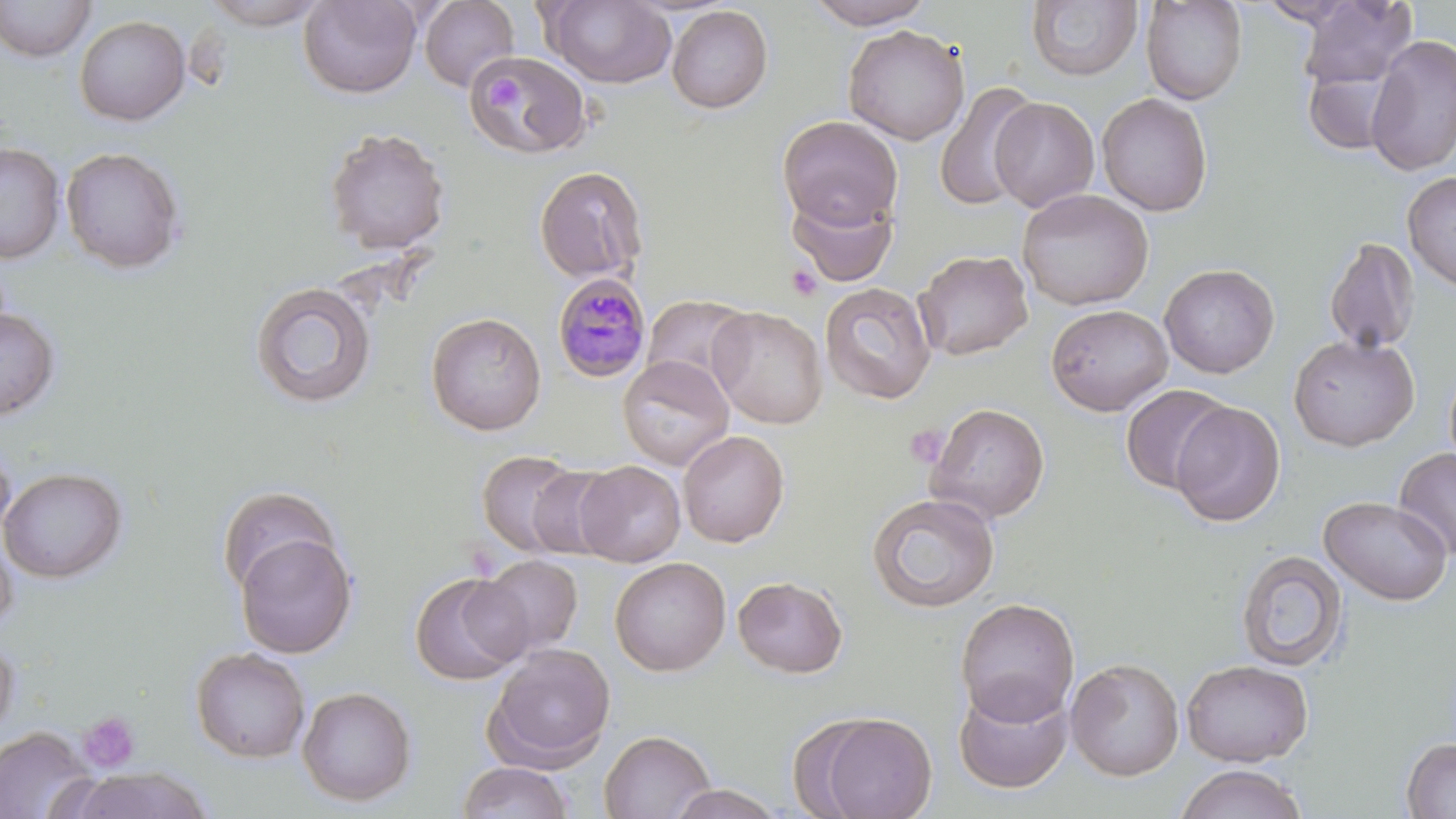
slide-level diagnosis = Plasmodium malariae
uninfected red blood cell locations = approximate bounding boxes as (x1, y1, x2, y2) in pixels: (0, 0, 96, 62), (201, 0, 329, 29), (298, 0, 422, 99), (804, 0, 935, 29), (1140, 0, 1248, 104), (1296, 0, 1417, 92), (419, 1, 520, 91), (543, 1, 677, 88), (1026, 1, 1142, 82), (1309, 1, 1442, 166), (666, 5, 774, 114), (73, 15, 190, 126), (842, 24, 970, 145), (1365, 34, 1456, 176), (466, 51, 591, 158), (1302, 62, 1402, 156), (933, 82, 1041, 211), (1096, 93, 1213, 216), (989, 97, 1100, 212), (777, 115, 903, 230), (324, 127, 450, 256), (0, 142, 65, 264), (60, 147, 186, 274), (534, 165, 649, 286), (1402, 170, 1456, 291), (1017, 188, 1154, 310), (787, 191, 898, 287), (1323, 236, 1420, 354), (913, 249, 1033, 361), (1159, 263, 1280, 378), (248, 280, 378, 410), (820, 282, 937, 405), (641, 294, 755, 393), (1046, 304, 1173, 416), (0, 306, 61, 422), (707, 306, 828, 429), (425, 312, 547, 436), (1288, 334, 1419, 451), (617, 354, 735, 471), (1119, 383, 1233, 495), (1169, 401, 1286, 527), (926, 403, 1050, 522), (677, 429, 790, 547), (0, 438, 17, 546), (1393, 448, 1456, 560), (477, 449, 585, 559), (574, 460, 686, 566), (525, 465, 623, 560), (0, 466, 128, 583), (217, 485, 342, 600), (866, 493, 1000, 613), (1318, 495, 1452, 606), (0, 531, 18, 639), (234, 531, 358, 658), (1236, 549, 1348, 672), (474, 555, 584, 659), (609, 556, 731, 677), (409, 571, 529, 686), (733, 575, 848, 678), (955, 597, 1080, 725), (0, 632, 19, 742), (484, 643, 616, 771), (190, 646, 310, 763), (1066, 658, 1184, 781), (1181, 659, 1313, 767), (954, 680, 1073, 795), (297, 686, 417, 806), (799, 711, 939, 818), (0, 725, 96, 818), (600, 729, 716, 819), (1401, 736, 1456, 818), (456, 762, 576, 819), (1175, 763, 1308, 819), (67, 766, 215, 818), (667, 784, 787, 819)
field of view = single
stain = May-Grünwald-Giemsa
image size = 1456×819 pixels
Plasmodium malariae-infected red blood cell locations = approximate bounding boxes as (x1, y1, x2, y2) in pixels: (552, 272, 652, 382)
modality = optical microscopy
magnification = 1000x
platelet locations = approximate bounding boxes as (x1, y1, x2, y2) in pixels: (484, 75, 523, 113), (786, 264, 822, 300), (906, 423, 949, 466), (78, 711, 141, 774)
preparation = thin blood film